Identify the blood parasite species.
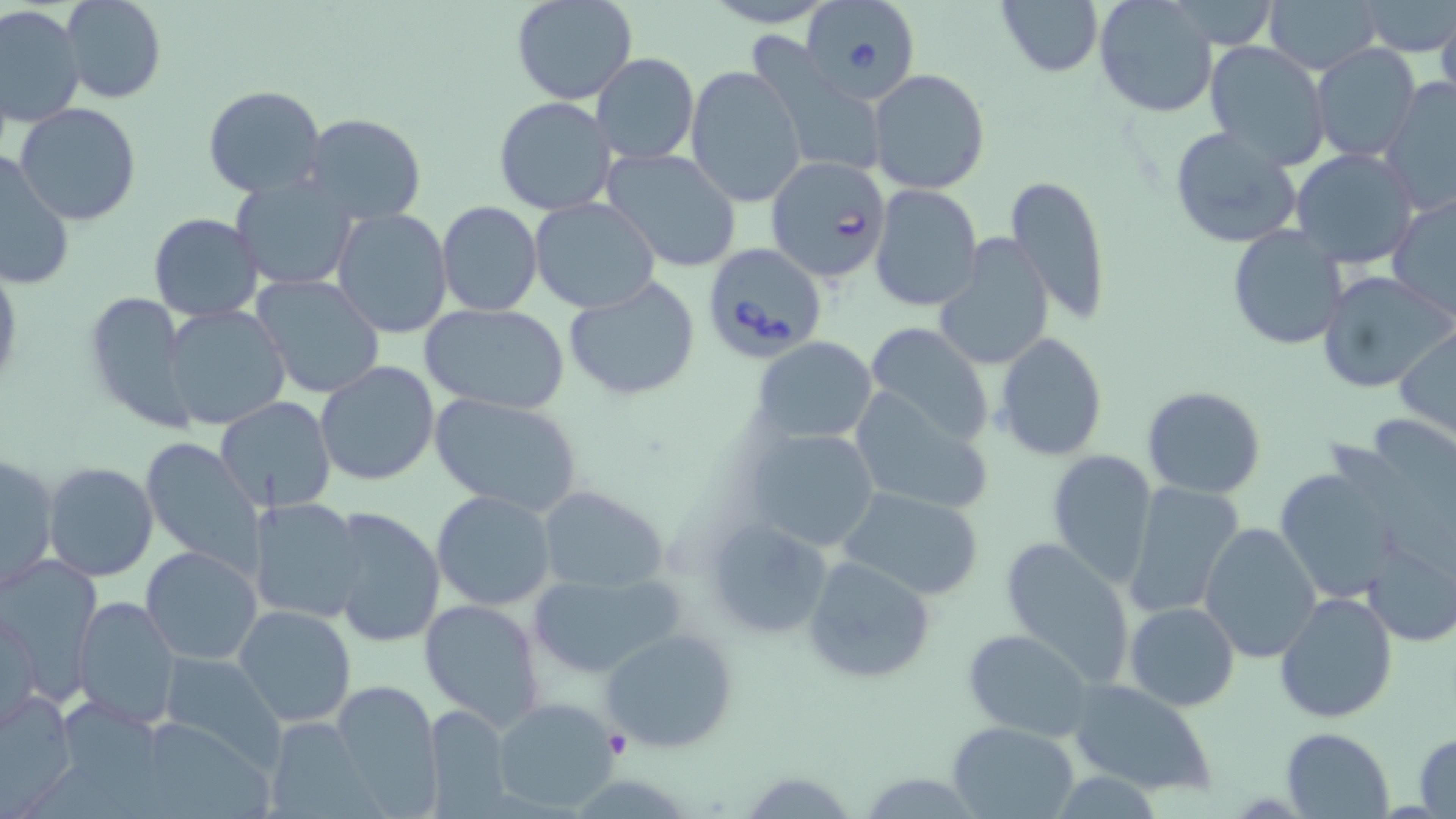
Babesia divergens.

Approximate bounding boxes as [x1, y1, x2, y2] in pixels. Babesia divergens-infected red blood cell locations: [809, 0, 923, 103], [765, 157, 890, 282], [700, 242, 832, 364]. Uninfected red blood cell locations: [63, 0, 166, 104], [511, 0, 638, 104], [696, 0, 841, 27], [994, 0, 1105, 79], [1092, 0, 1217, 118], [1264, 0, 1383, 73], [1360, 1, 1454, 56], [1159, 2, 1284, 46], [0, 5, 85, 128], [1436, 11, 1456, 106], [751, 34, 888, 171], [1204, 41, 1331, 170], [1310, 43, 1422, 162], [591, 53, 699, 164], [687, 67, 805, 207], [868, 68, 993, 195], [1380, 77, 1456, 217], [203, 84, 327, 199], [494, 96, 618, 217], [16, 103, 141, 225], [299, 113, 428, 226], [1168, 124, 1304, 251], [1290, 146, 1420, 267], [602, 148, 741, 273], [0, 152, 75, 291], [1006, 174, 1112, 325], [233, 176, 360, 291], [869, 184, 983, 311], [1388, 193, 1456, 323], [530, 197, 659, 313], [436, 202, 544, 317], [332, 207, 452, 337], [148, 213, 263, 323], [1226, 225, 1348, 349], [935, 237, 1054, 370], [962, 266, 1100, 439], [1316, 270, 1453, 395], [252, 273, 386, 399], [563, 277, 701, 402], [82, 290, 197, 432], [161, 303, 290, 429], [421, 305, 569, 414], [860, 320, 994, 451], [1394, 328, 1456, 438], [992, 332, 1108, 462], [754, 336, 875, 444], [316, 361, 440, 486], [851, 386, 994, 517], [1142, 386, 1267, 498], [429, 393, 582, 515], [216, 396, 335, 512], [742, 428, 883, 553], [140, 437, 260, 577], [1046, 449, 1158, 587], [0, 452, 59, 593], [43, 462, 159, 584], [1276, 468, 1403, 601], [1124, 482, 1247, 619], [538, 486, 668, 592], [838, 486, 988, 600], [431, 490, 557, 611], [251, 499, 370, 624], [326, 508, 445, 647], [700, 515, 834, 642], [1198, 522, 1322, 664], [997, 535, 1136, 686], [1362, 539, 1455, 645], [141, 545, 262, 667], [803, 555, 936, 686], [2, 557, 104, 702], [525, 569, 688, 681], [1274, 590, 1398, 723], [71, 595, 180, 727], [419, 597, 547, 731], [1124, 602, 1239, 711], [234, 603, 357, 729], [1, 605, 43, 734], [601, 627, 739, 754], [962, 629, 1094, 741], [160, 652, 287, 773], [1066, 677, 1217, 797], [331, 680, 443, 812], [2, 690, 76, 806], [491, 696, 621, 810], [421, 702, 514, 816], [127, 716, 279, 818], [948, 723, 1078, 818], [1280, 727, 1395, 819], [1412, 733, 1456, 817]. Platelet locations: [602, 729, 628, 758]. Optical microscopy. Thin blood film. Image is 1456×819 pixels. 1000x magnification. May-Grünwald-Giemsa-stained preparation. One field of a larger specimen.